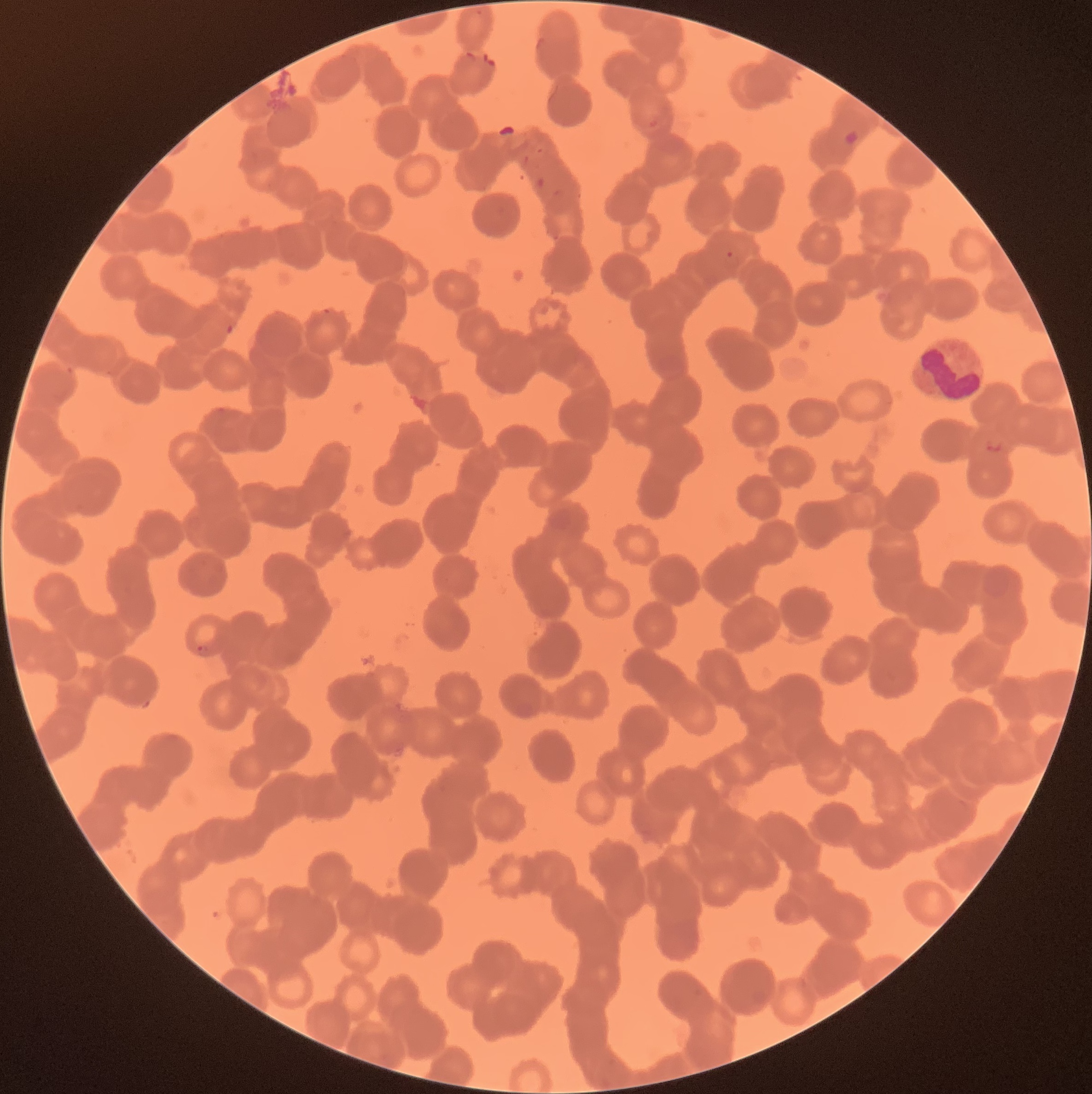
coordinate format = approximate bounding boxes as named x1/y1/x2/y2 corners in pixels
white blood cell locations = (x1=909, y1=333, x2=987, y2=400)
Plasmodium parasite locations = (x1=722, y1=249, x2=739, y2=268), (x1=984, y1=439, x2=1004, y2=453), (x1=196, y1=645, x2=209, y2=654)
modality = light microscopy
red blood cell morphology = rouleaux formation
image size = 1092×1094 pixels
preparation = thin blood smear